Locate every leukocyte (white blood cell).
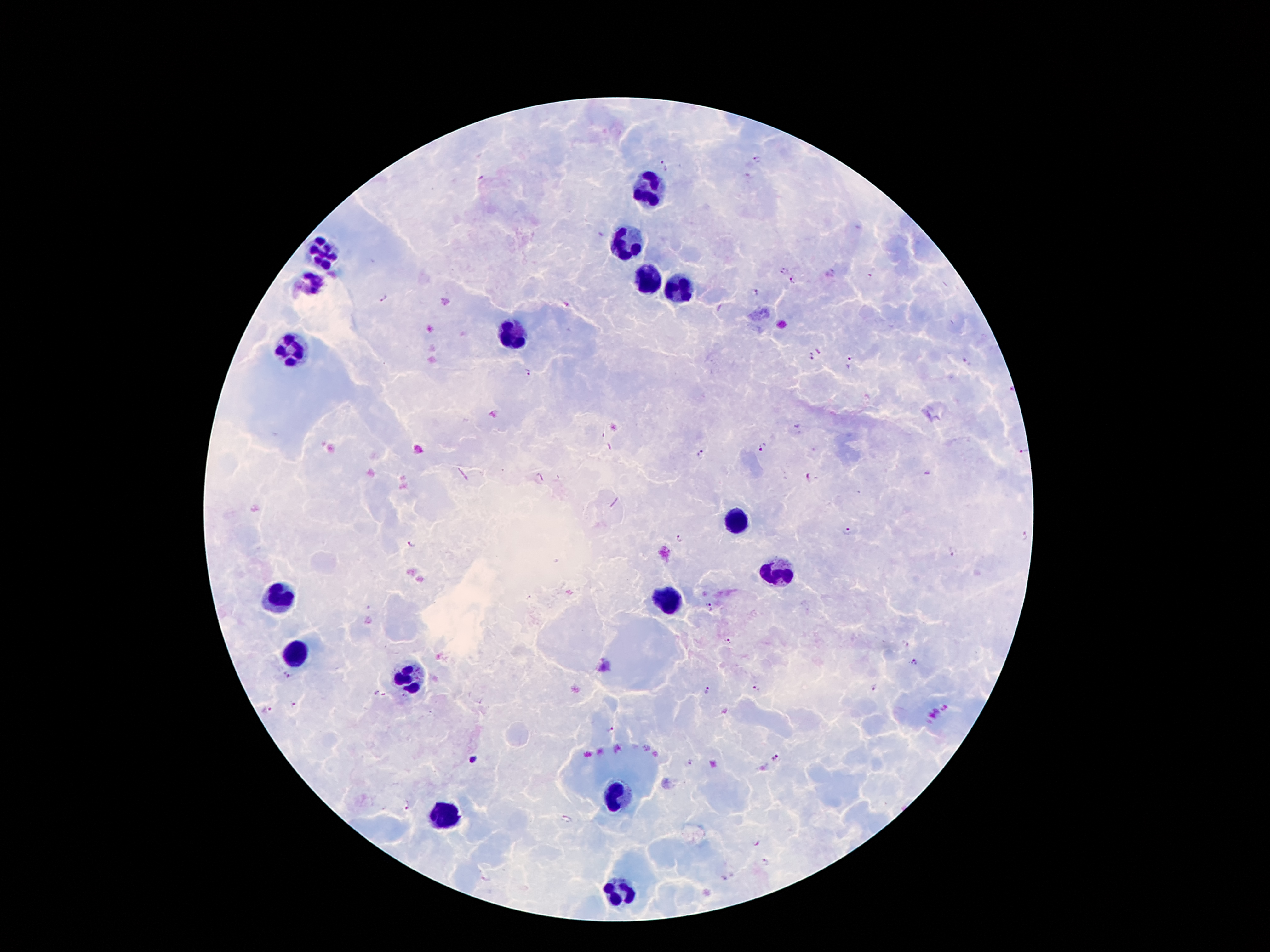
Approximate centers as [x, y] in pixels.
Leukocytes: [650, 187], [629, 243], [320, 253], [649, 280], [311, 282], [677, 289], [512, 337], [290, 348], [736, 521], [778, 573], [282, 597], [670, 602], [293, 655], [406, 681], [616, 796], [444, 815], [621, 893].

Malaria parasite locations: [758, 161], [663, 165], [785, 269], [869, 277], [794, 280], [756, 291], [382, 298], [819, 350], [810, 356], [850, 362], [965, 362], [528, 371], [761, 446], [1022, 453], [700, 454], [808, 477], [849, 530], [1025, 535], [681, 537], [412, 543], [951, 550], [711, 607], [728, 641], [905, 644], [912, 663], [288, 674], [874, 689], [708, 690], [756, 690], [380, 694], [294, 705], [265, 709], [610, 730], [776, 757], [472, 760], [691, 763], [407, 805], [566, 818], [765, 862]. Giemsa-stained preparation. Patient malaria status: infected with Plasmodium falciparum. Photographed through the microscope eyepiece with a smartphone camera. Thick peripheral-blood smear. 100x magnification. Image is 1270×952 pixels. One field from this slide.